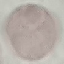

result = no malaria parasites seen
capture = smartphone camera at the microscope eyepiece
preparation = thin blood smear
stain = Giemsa
image type = automatically extracted cell patch, resized to 64 × 64 pixels